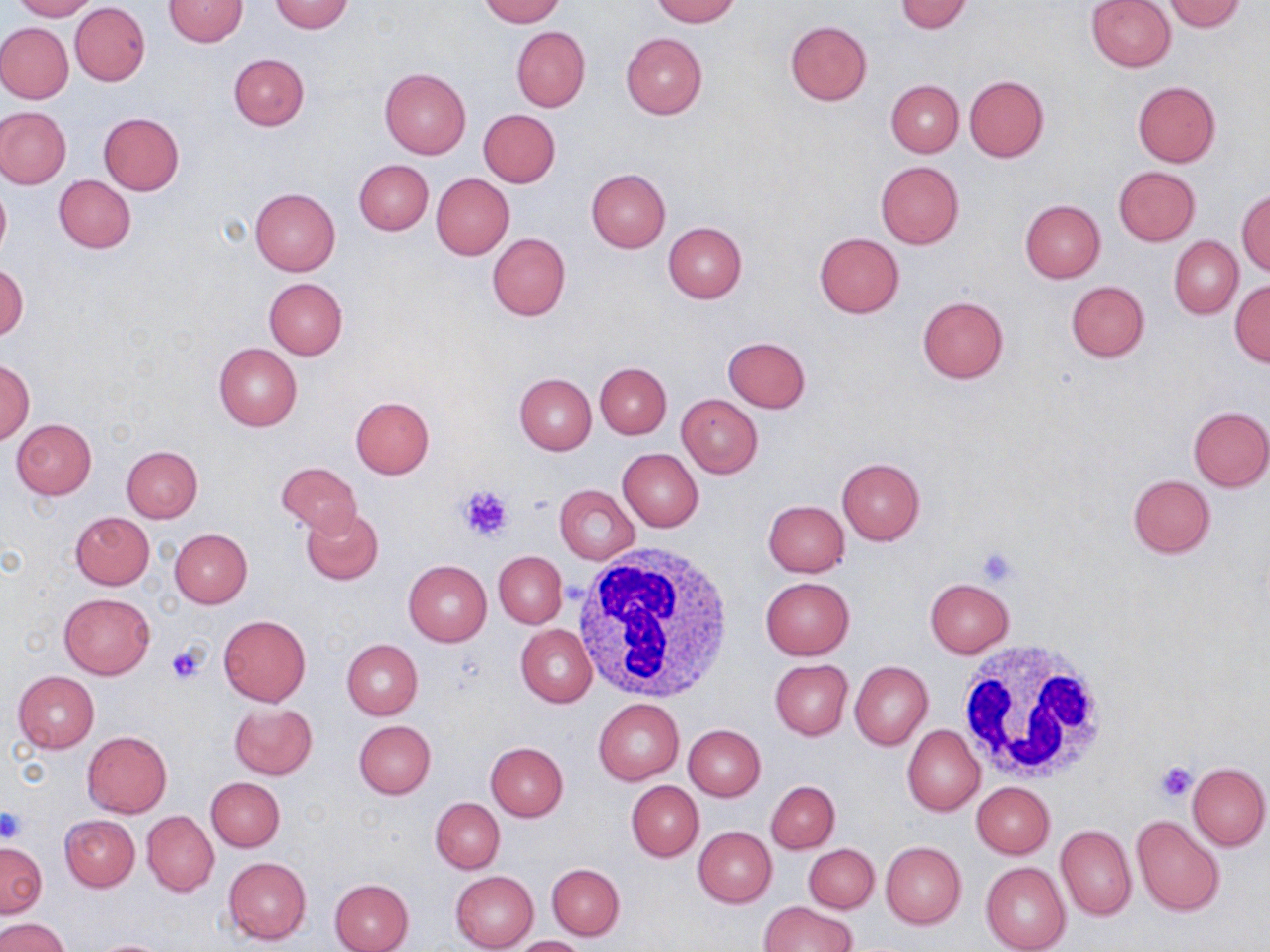
{
  "slide_level_diagnosis": "negative for blood parasites",
  "platelet_locations": "approximate bounding boxes as (x1, y1, x2, y2) in pixels: (458, 485, 513, 541), (976, 546, 1019, 585), (166, 642, 208, 684), (1154, 761, 1198, 803), (0, 807, 25, 842)",
  "image_size": "1270×952 pixels",
  "stain": "May-Grünwald-Giemsa",
  "uninfected_red_blood_cell_locations": "approximate bounding boxes as (x1, y1, x2, y2) in pixels: (11, 0, 97, 20), (164, 0, 249, 47), (269, 0, 354, 33), (479, 0, 564, 26), (652, 0, 739, 25), (1086, 0, 1175, 72), (896, 1, 974, 34), (1164, 1, 1246, 32), (70, 2, 150, 86), (786, 20, 872, 104), (0, 23, 73, 102), (511, 26, 590, 111), (621, 33, 707, 118), (228, 53, 309, 130), (380, 68, 471, 158), (964, 75, 1049, 162), (886, 80, 963, 157), (1133, 81, 1221, 166), (0, 108, 71, 188), (479, 109, 561, 187), (98, 113, 184, 195), (353, 158, 433, 235), (876, 161, 964, 248), (1113, 166, 1201, 246), (585, 168, 672, 253), (431, 174, 514, 260), (55, 175, 136, 253), (0, 181, 10, 262), (250, 186, 341, 276), (1237, 189, 1270, 275), (1020, 199, 1106, 282), (662, 220, 747, 303), (486, 232, 570, 321), (814, 233, 904, 317), (1170, 236, 1242, 318), (0, 263, 28, 341), (264, 278, 347, 358), (1229, 279, 1269, 367), (1066, 280, 1149, 362), (917, 295, 1009, 383), (721, 336, 811, 413), (213, 343, 302, 431), (1, 358, 35, 446), (595, 364, 671, 438), (514, 373, 596, 453), (676, 394, 762, 478), (350, 396, 434, 479), (1188, 406, 1270, 490), (10, 418, 96, 499), (122, 446, 203, 522), (618, 448, 703, 531), (836, 458, 926, 544), (275, 462, 363, 536), (1128, 475, 1215, 558), (555, 484, 639, 564), (763, 500, 849, 576), (301, 506, 384, 584), (70, 512, 154, 589), (169, 528, 252, 607), (495, 552, 566, 629), (403, 559, 492, 645), (760, 577, 855, 659), (925, 578, 1014, 657), (60, 592, 154, 678), (218, 614, 311, 706), (517, 624, 597, 706), (341, 638, 423, 719), (770, 659, 852, 738), (850, 660, 932, 750), (13, 671, 99, 753), (594, 698, 684, 784), (228, 702, 318, 780), (354, 719, 436, 798), (902, 724, 985, 816), (683, 725, 766, 800), (83, 731, 172, 817), (485, 742, 568, 821), (1186, 761, 1269, 850), (206, 777, 285, 851), (767, 780, 839, 854), (626, 781, 703, 861), (972, 782, 1054, 858), (431, 798, 504, 873), (142, 811, 219, 896), (60, 815, 139, 891), (1132, 815, 1225, 916), (1055, 825, 1136, 921), (693, 826, 776, 907), (1, 842, 46, 918), (881, 842, 966, 928), (804, 844, 879, 913), (223, 857, 311, 945), (981, 862, 1070, 952), (547, 863, 625, 939), (451, 871, 538, 952), (329, 878, 414, 952), (758, 901, 855, 952), (0, 918, 69, 952), (512, 935, 589, 952), (87, 939, 176, 952)",
  "preparation": "thin blood smear",
  "field_of_view": "one of a larger specimen",
  "modality": "light microscopy",
  "white_blood_cell_locations": "approximate bounding boxes as (x1, y1, x2, y2) in pixels: (573, 545, 734, 704), (952, 638, 1114, 788)",
  "magnification": "1000x"
}